Report the malaria status of this cell.
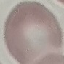

It is uninfected.

preparation = thin smear
capture = smartphone camera at the microscope eyepiece
image type = cell patch, automatically extracted from a larger field of view and resized to 64 × 64 pixels
stain = Giemsa